Describe the morphology of the red blood cells.
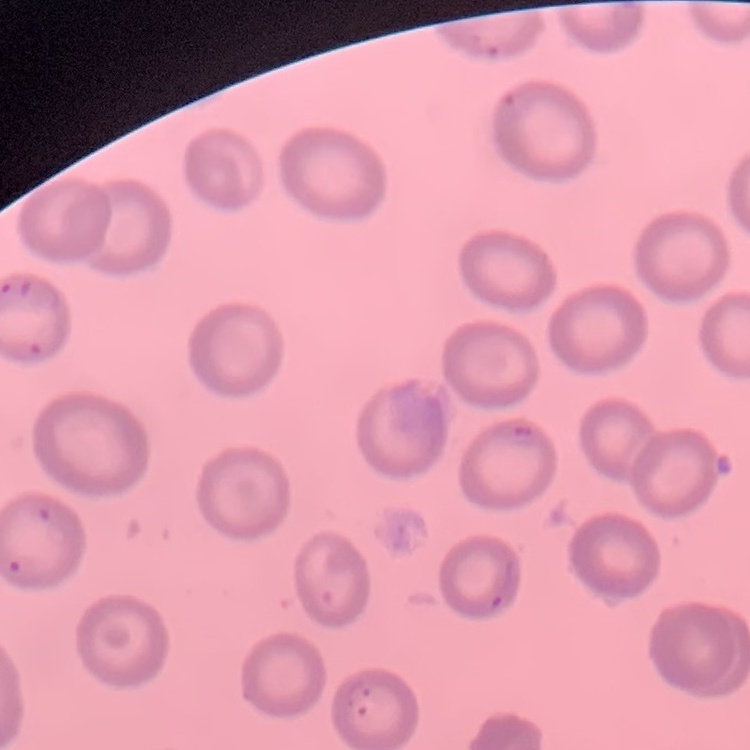
They show no rouleaux formation.

Stained with either Field's or Giemsa. One tile cut from a larger photomicrograph. Thin blood film.